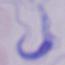
Summary:
  - Identification: trypanosome
  - Modality: photomicrograph
  - Magnification: 1000x